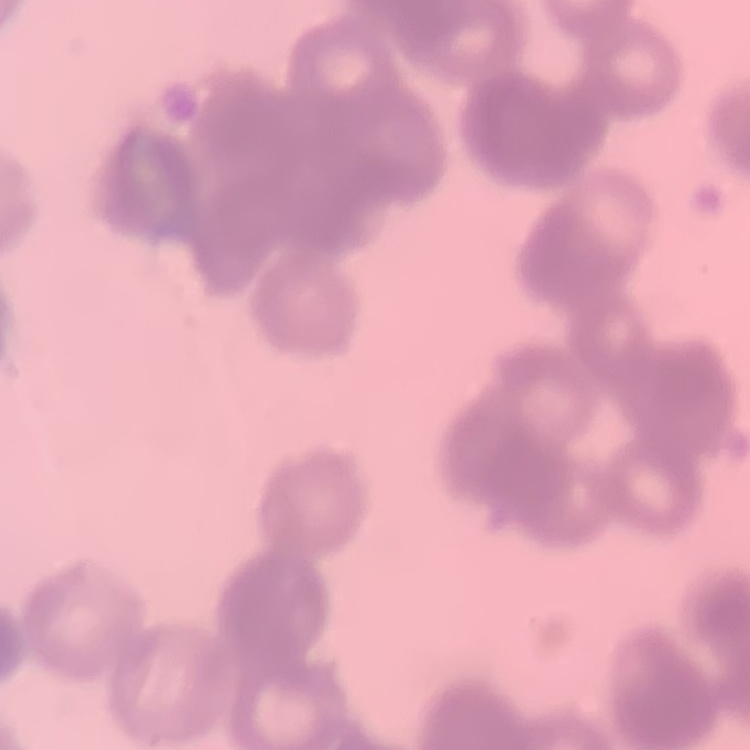 The erythrocytes exhibit rouleaux formation. Thin blood smear. One tile cut from a larger photomicrograph. Field's or Giemsa stain.